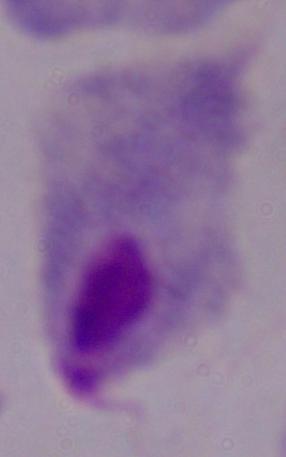
magnification: 1000x
modality: micrograph
identification: trichomonad